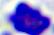

Summary:
  - Modality: micrograph
  - Magnification: 400x
  - Identification: leukocyte